Give the position of every malaria parasite and every leukocyte.
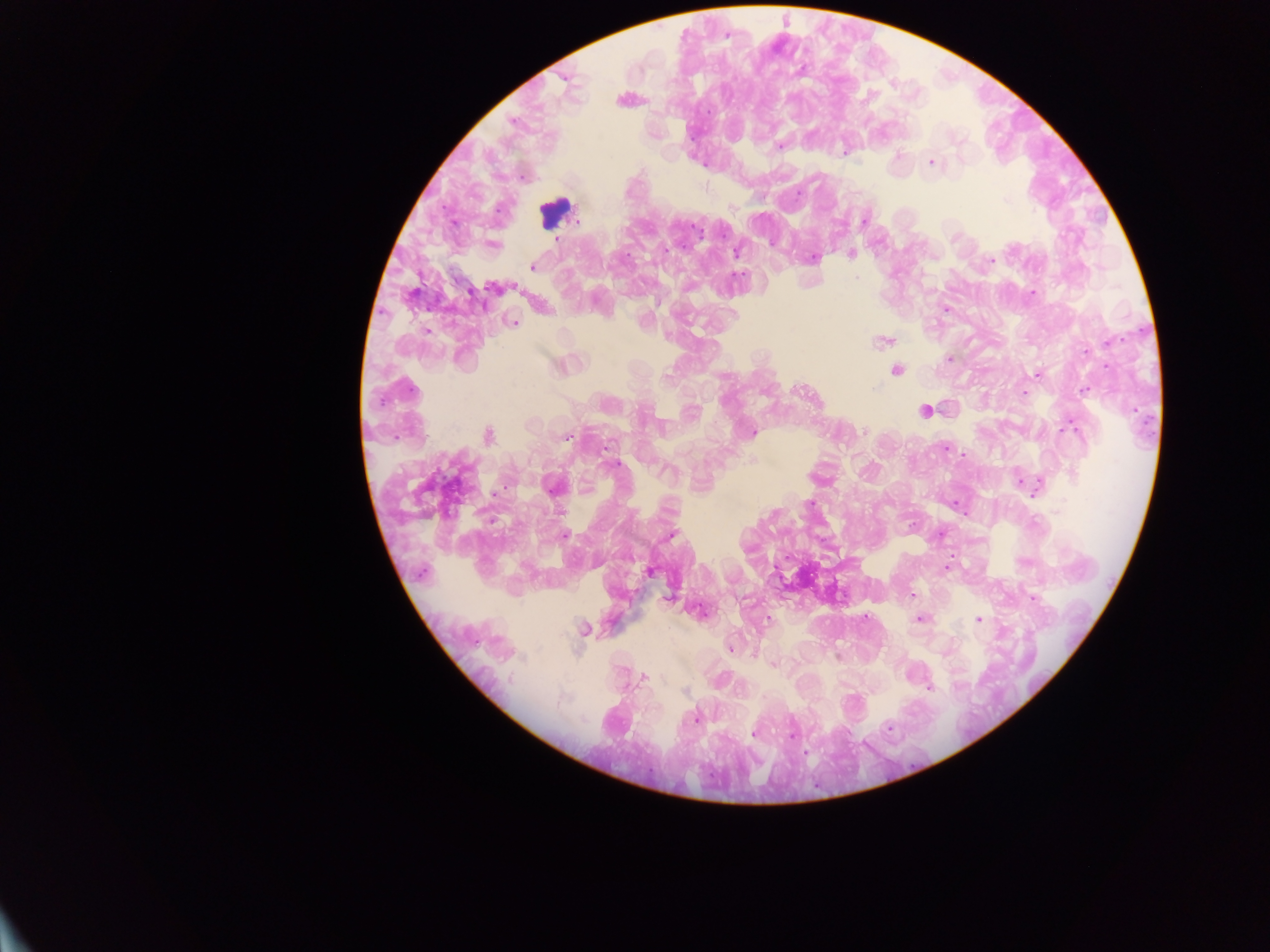
Approximate centers as (x, y) in pixels.
Malaria parasites: (726, 35), (708, 113), (512, 121), (959, 141), (779, 147), (844, 153), (931, 162), (1005, 200), (732, 207), (578, 220), (864, 221), (557, 239), (664, 249), (737, 253), (852, 254), (813, 258), (992, 260), (532, 268), (737, 275), (857, 278), (497, 287), (1032, 293), (945, 310), (513, 323), (426, 331), (883, 342), (1111, 342), (1086, 351), (950, 358), (1106, 366), (1036, 374), (875, 388), (411, 390), (1084, 390), (1024, 394), (1070, 428), (864, 431), (752, 433), (488, 435), (566, 437), (945, 448), (613, 464), (1021, 481), (554, 487), (1035, 488), (558, 511), (772, 514), (565, 535), (671, 535), (947, 567), (649, 572), (912, 595), (1032, 598), (769, 619), (920, 619), (978, 619), (585, 629), (730, 649), (773, 665), (643, 677), (929, 688), (685, 692), (697, 717), (888, 727), (792, 731), (754, 733).
Leukocytes: (556, 213), (894, 370), (927, 408).

One field of view. Thick blood film. Sample from Ghana. Image is 1270×952 pixels. Mobile-phone photograph taken through the microscope.